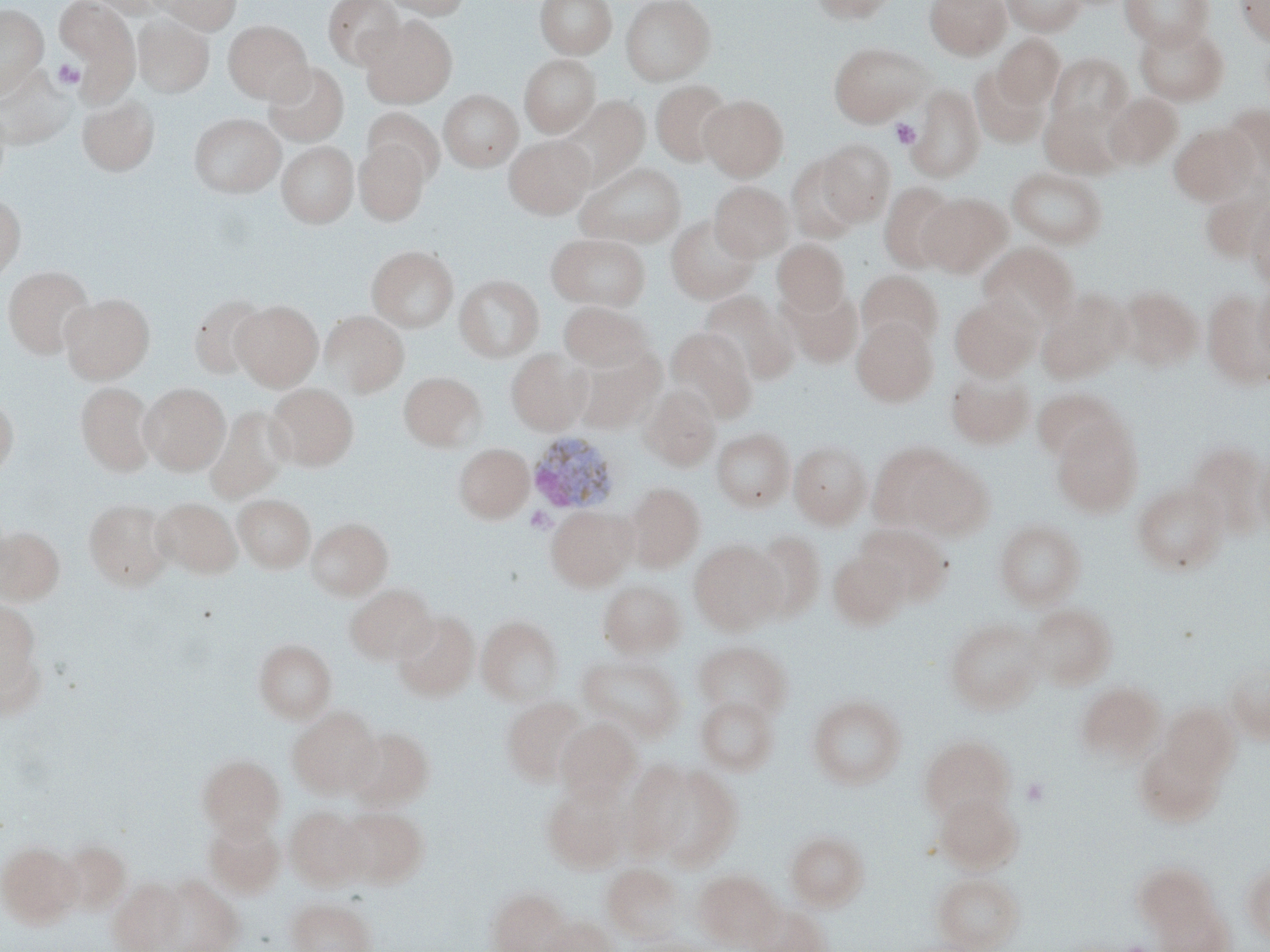

Approximate bounding boxes as (x1, y1, x2, y2) in pixels. Platelet locations: (52, 59, 84, 90), (891, 119, 921, 149), (525, 507, 555, 533), (1021, 776, 1051, 807). Plasmodium ovale-infected red blood cell locations: (526, 431, 621, 515). Uninfected red blood cell locations: (55, 0, 136, 69), (90, 0, 160, 18), (156, 0, 242, 34), (322, 0, 406, 70), (381, 0, 471, 19), (535, 0, 617, 59), (620, 0, 715, 85), (808, 0, 898, 23), (925, 0, 1011, 60), (1000, 0, 1086, 36), (1120, 0, 1213, 50), (1235, 0, 1270, 46), (0, 4, 48, 96), (133, 14, 214, 97), (361, 16, 457, 108), (223, 20, 312, 103), (1134, 22, 1229, 105), (994, 34, 1065, 110), (827, 41, 932, 126), (1047, 53, 1132, 132), (519, 54, 600, 136), (263, 62, 349, 146), (0, 65, 74, 149), (969, 66, 1049, 148), (651, 80, 734, 167), (906, 84, 984, 182), (439, 89, 522, 172), (1105, 93, 1183, 170), (700, 95, 788, 180), (77, 96, 160, 175), (561, 96, 649, 186), (1040, 100, 1126, 179), (1219, 104, 1270, 188), (363, 107, 444, 185), (189, 113, 285, 197), (1169, 123, 1255, 205), (505, 135, 593, 218), (816, 139, 896, 226), (354, 140, 429, 225), (277, 141, 358, 228), (786, 153, 864, 243), (576, 161, 686, 248), (1006, 167, 1108, 248), (710, 181, 793, 261), (878, 182, 961, 272), (920, 192, 1012, 277), (0, 193, 25, 284), (1246, 193, 1270, 290), (666, 214, 759, 304), (547, 232, 650, 310), (772, 239, 850, 315), (978, 243, 1079, 330), (367, 245, 458, 332), (3, 266, 95, 359), (857, 270, 943, 352), (454, 274, 544, 362), (1253, 280, 1270, 375), (779, 284, 864, 368), (1117, 286, 1203, 371), (1036, 288, 1130, 383), (700, 290, 797, 385), (1202, 290, 1270, 389), (60, 293, 154, 383), (189, 294, 270, 379), (949, 294, 1040, 380), (232, 301, 322, 390), (559, 302, 652, 370), (320, 310, 409, 396), (852, 318, 938, 406), (666, 328, 758, 423), (506, 348, 591, 434), (575, 350, 663, 433), (946, 367, 1035, 449), (400, 371, 485, 450), (76, 382, 156, 476), (139, 382, 230, 475), (266, 383, 358, 471), (640, 386, 721, 470), (1033, 387, 1124, 463), (0, 395, 18, 481), (205, 406, 290, 503), (1051, 415, 1143, 517), (712, 428, 795, 512), (789, 439, 871, 528), (867, 442, 957, 532), (1188, 442, 1268, 540), (454, 443, 534, 522), (1253, 451, 1270, 532), (910, 456, 994, 538), (625, 482, 705, 570), (1132, 482, 1228, 576), (234, 494, 315, 572), (153, 497, 242, 578), (84, 498, 174, 590), (545, 506, 635, 591), (307, 518, 392, 600), (994, 519, 1086, 609), (857, 524, 951, 605), (0, 526, 64, 604), (749, 530, 826, 622), (689, 540, 784, 634), (828, 550, 909, 630), (598, 580, 686, 657), (345, 584, 436, 664), (0, 599, 46, 714), (1026, 603, 1117, 689), (393, 610, 479, 700), (477, 615, 563, 705), (945, 618, 1043, 713), (254, 639, 336, 723), (693, 641, 790, 722), (579, 654, 684, 742), (1224, 661, 1270, 744), (1075, 682, 1164, 765), (808, 694, 907, 789), (696, 695, 779, 775), (501, 696, 585, 784), (1160, 704, 1239, 786), (288, 706, 382, 798), (556, 718, 639, 797), (346, 726, 434, 809), (919, 734, 1015, 823), (1135, 737, 1226, 827), (198, 755, 285, 837), (643, 762, 743, 868), (543, 781, 630, 872), (933, 791, 1023, 873), (285, 806, 368, 889), (337, 807, 428, 887), (204, 816, 284, 896), (786, 830, 869, 910), (60, 840, 130, 913), (0, 842, 81, 927), (1134, 862, 1217, 932), (602, 863, 684, 941), (1242, 864, 1270, 942), (693, 870, 781, 950), (932, 872, 1023, 952), (146, 875, 241, 951), (108, 877, 187, 951), (484, 887, 570, 952), (286, 896, 376, 952), (1154, 899, 1233, 952), (747, 903, 830, 952), (537, 914, 616, 952). Slide-level diagnosis: Plasmodium ovale. Image is 1270×952 pixels. May-Grünwald-Giemsa stain. Thin blood smear. Captured at 1000x magnification. One field of a larger specimen. Optical microscopy.